Classify this cell by malaria status.
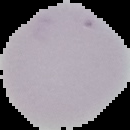
It is uninfected.

Summary:
  - Image type: cell region segmented out of the field of view; surrounding area masked to black
  - Image size: 130×130 pixels
  - Preparation: thin blood smear